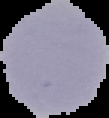

image type = cell region segmented out of the field of view; surrounding area masked to black
preparation = thin blood film
image size = 109×118 pixels
malaria status = uninfected